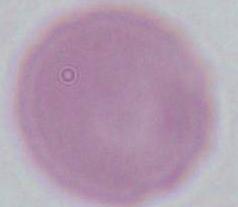
{
  "modality": "photomicrograph",
  "identification": "red blood cell",
  "magnification": "1000x"
}